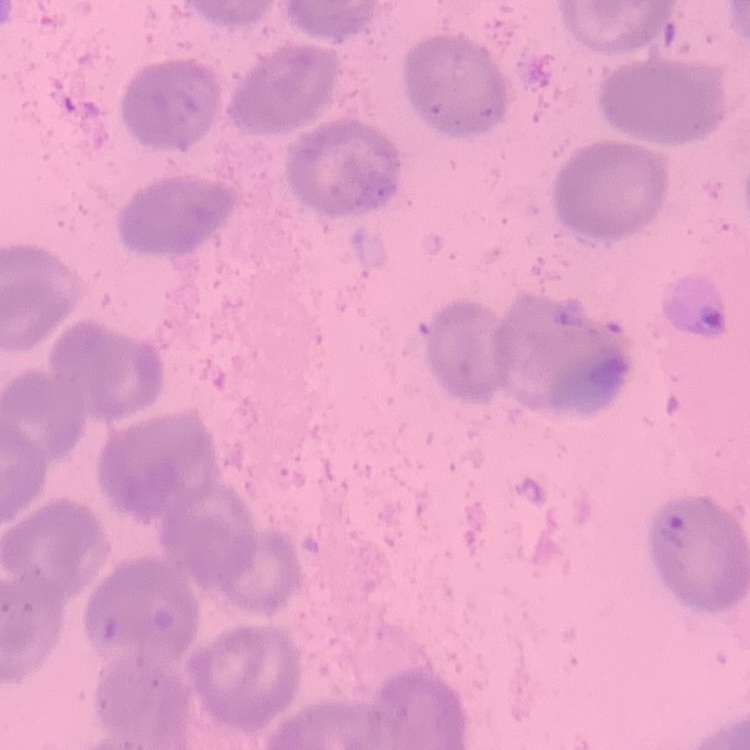
Summary:
  - Red blood cell morphology: no rouleaux formation
  - Stain: Field's or Giemsa
  - Preparation: thin blood smear
  - Image type: square crop of a larger photomicrograph